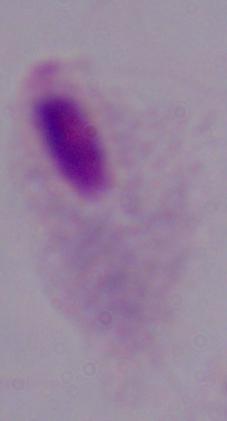
magnification = 1000x
modality = photomicrograph
identification = trichomonad